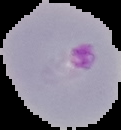
Malaria status: parasitized. Cell region segmented out of the field of view; the surrounding area is masked to black. From a thin blood film. Image is 121×130 pixels.